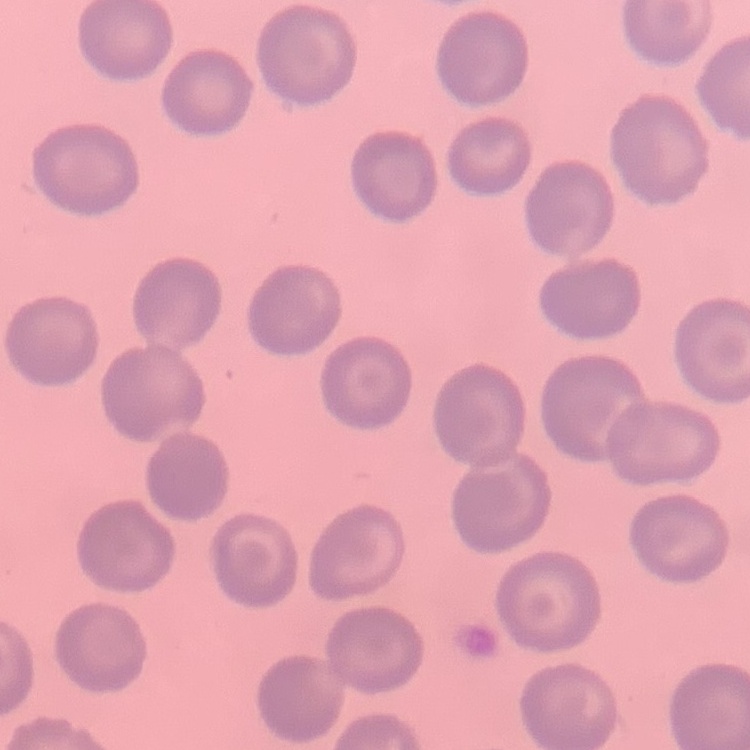
The red blood cells exhibit no rouleaux formation. One tile cut from a larger photomicrograph. Thin peripheral smear. Stained with either Field's or Giemsa.